Identify the parasite.
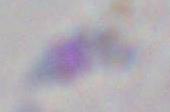

This is Toxoplasma gondii.

{
  "magnification": "1000x",
  "modality": "photomicrograph"
}